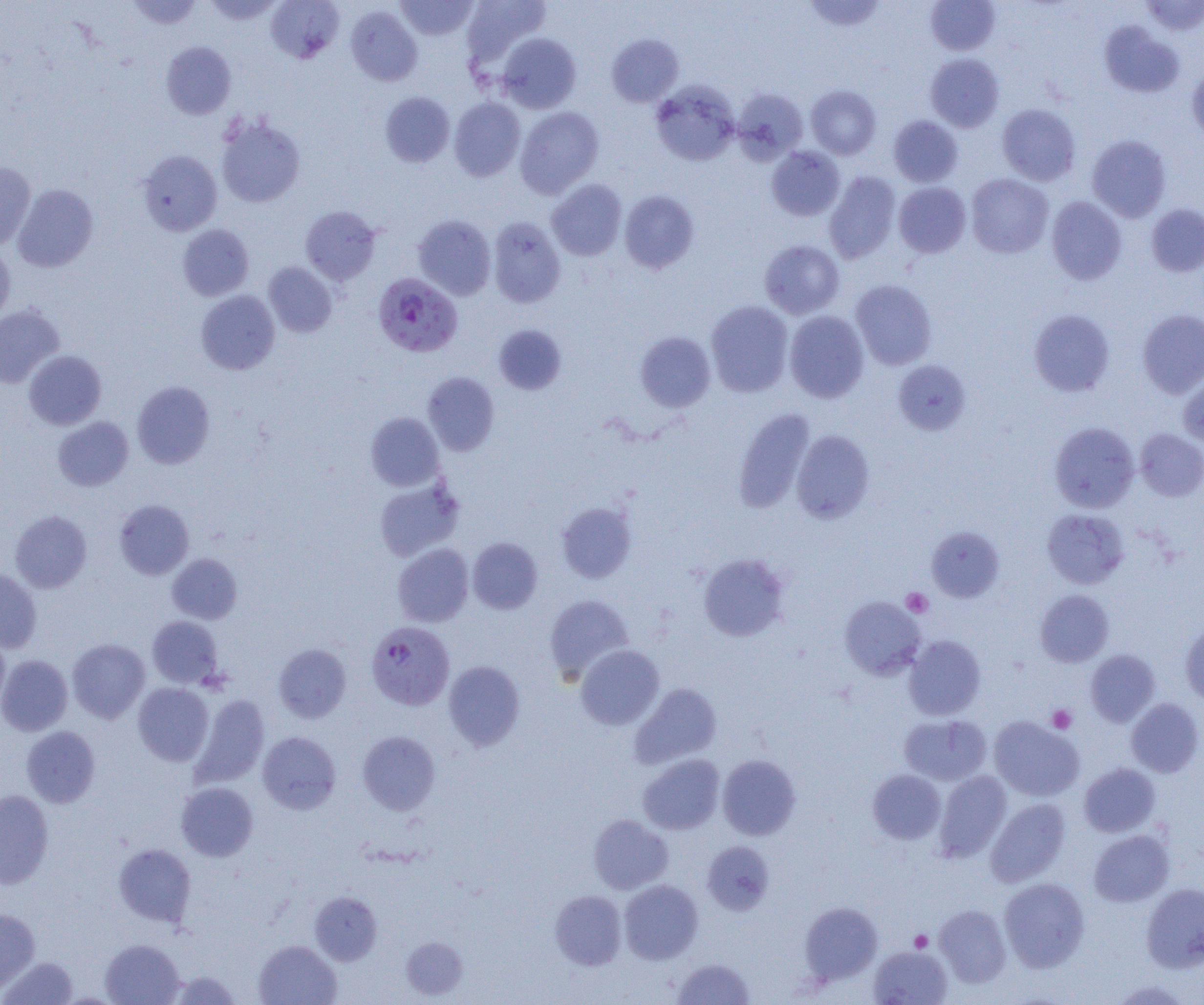
Approximate bounding boxes as (x1, y1, x2, y2) in pixels. Plasmodium falciparum-infected red blood cell locations: (373, 272, 462, 357), (366, 620, 455, 711). Uninfected red blood cell locations: (127, 0, 203, 30), (203, 0, 283, 24), (266, 0, 344, 63), (396, 0, 478, 40), (462, 0, 552, 70), (804, 0, 886, 32), (1141, 0, 1204, 36), (926, 1, 1000, 55), (346, 6, 423, 86), (1099, 20, 1184, 98), (497, 33, 582, 114), (607, 34, 684, 107), (161, 41, 237, 119), (925, 53, 1004, 132), (1187, 65, 1204, 142), (651, 81, 740, 166), (806, 85, 881, 159), (732, 87, 809, 164), (380, 91, 455, 168), (449, 97, 525, 181), (997, 104, 1080, 186), (515, 106, 604, 198), (215, 115, 305, 208), (888, 115, 963, 187), (1086, 135, 1171, 222), (767, 146, 845, 221), (137, 150, 222, 236), (0, 162, 36, 250), (824, 172, 900, 264), (966, 173, 1053, 258), (546, 179, 627, 261), (894, 182, 971, 258), (13, 185, 98, 272), (619, 190, 699, 273), (1046, 196, 1127, 284), (1146, 204, 1204, 277), (300, 205, 381, 285), (412, 215, 496, 300), (488, 216, 566, 308), (177, 224, 254, 301), (759, 240, 845, 319), (0, 243, 16, 325), (264, 262, 337, 337), (850, 280, 937, 370), (196, 290, 280, 375), (706, 300, 793, 397), (0, 303, 65, 388), (1028, 309, 1115, 397), (1138, 309, 1204, 398), (784, 311, 869, 402), (493, 324, 567, 394), (635, 331, 715, 412), (23, 350, 107, 430), (893, 359, 971, 435), (422, 372, 500, 456), (1178, 374, 1204, 451), (132, 381, 215, 468), (733, 408, 815, 513), (365, 412, 445, 491), (53, 416, 133, 491), (1049, 422, 1139, 512), (1135, 428, 1204, 501), (791, 430, 875, 523), (374, 478, 464, 561), (114, 500, 194, 579), (556, 502, 636, 583), (1041, 508, 1129, 589), (10, 510, 92, 593), (926, 527, 1004, 603), (467, 537, 543, 614), (392, 543, 474, 627), (167, 553, 242, 624), (698, 553, 789, 641), (0, 568, 42, 653), (1035, 589, 1114, 667), (544, 594, 634, 680), (840, 596, 925, 679), (147, 616, 223, 688), (1181, 621, 1204, 706), (0, 635, 10, 712), (904, 635, 986, 720), (67, 638, 150, 723), (273, 644, 351, 723), (575, 645, 664, 730), (1085, 649, 1160, 727), (0, 655, 72, 736), (443, 660, 525, 750), (133, 683, 213, 766), (630, 683, 722, 769), (190, 694, 269, 788), (1126, 698, 1203, 777), (899, 714, 991, 785), (989, 716, 1084, 801), (21, 726, 100, 808), (357, 730, 441, 815), (258, 731, 341, 814), (638, 754, 725, 835), (718, 755, 801, 840), (1079, 763, 1160, 837), (867, 769, 945, 844), (934, 771, 1011, 862), (176, 781, 258, 862), (0, 789, 54, 888), (986, 798, 1070, 886), (588, 814, 673, 894), (1088, 829, 1174, 907), (702, 841, 774, 915), (113, 843, 196, 927), (999, 877, 1090, 972), (619, 880, 703, 964), (1141, 883, 1204, 972), (550, 890, 627, 970), (310, 891, 382, 965), (800, 902, 882, 984), (934, 905, 1011, 987), (0, 908, 40, 993), (401, 936, 468, 1000), (100, 938, 185, 1005), (254, 940, 342, 1005), (869, 945, 953, 1004), (1, 956, 78, 1004), (672, 958, 756, 1004), (168, 970, 241, 1004), (1111, 980, 1194, 1005). Platelet locations: (901, 588, 933, 617), (1047, 705, 1077, 733), (910, 931, 933, 953). Slide-level diagnosis: Plasmodium falciparum. Image is 1204×1005 pixels. 1000x magnification. Optical microscopy. Thin blood film. One field of a larger specimen.